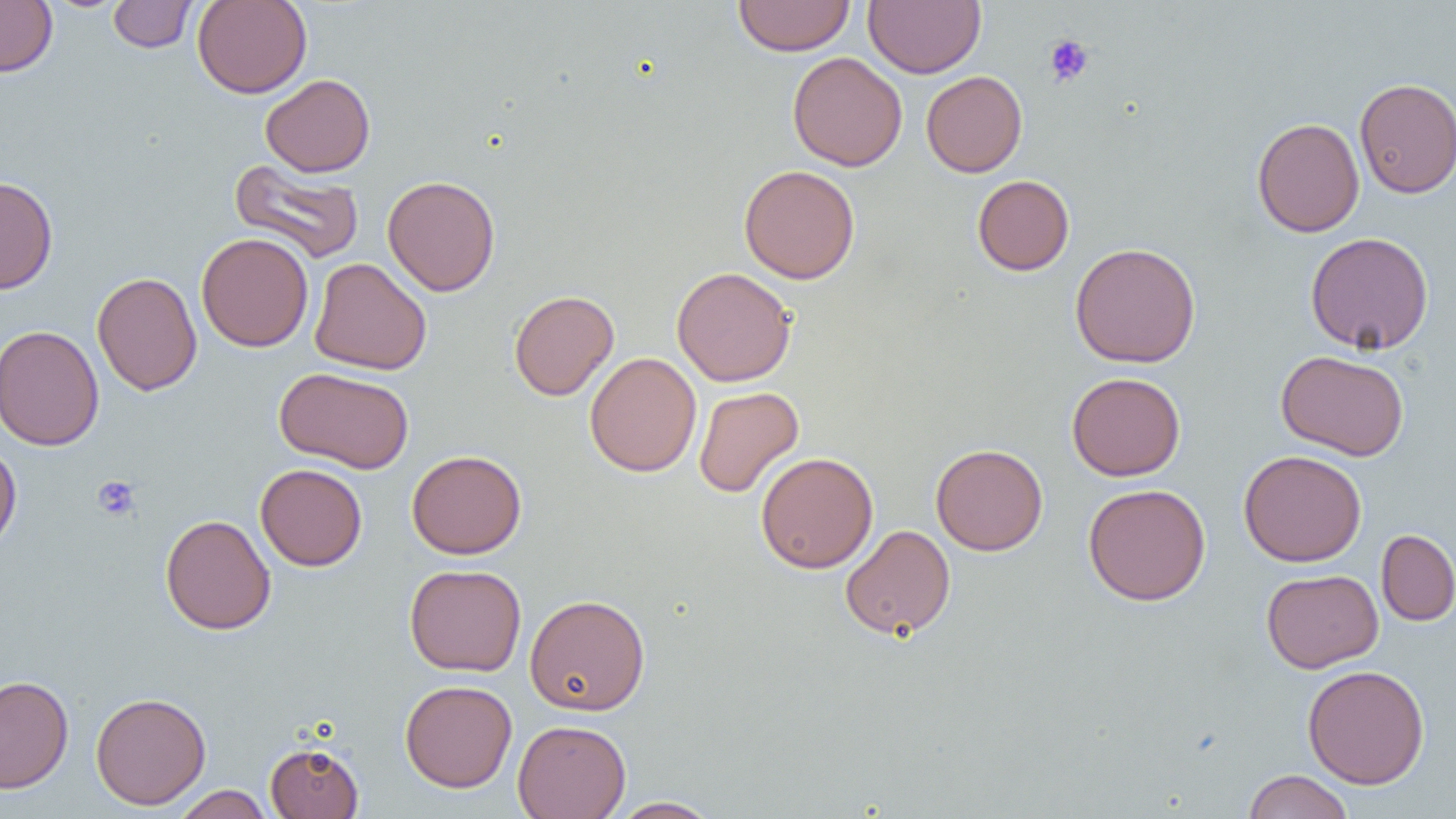 Approximate bounding boxes as (x1, y1, x2, y2) in pixels. Platelet locations: (1044, 34, 1093, 86), (92, 476, 141, 521). Uninfected red blood cell locations: (0, 0, 58, 77), (108, 0, 197, 53), (192, 0, 312, 98), (733, 0, 855, 56), (864, 0, 985, 78), (787, 52, 907, 171), (921, 71, 1028, 177), (261, 74, 375, 177), (1354, 78, 1456, 198), (1251, 117, 1365, 237), (229, 158, 365, 265), (739, 165, 860, 284), (383, 174, 500, 296), (972, 174, 1074, 275), (0, 176, 58, 295), (1304, 231, 1434, 355), (196, 233, 313, 352), (1070, 242, 1201, 367), (309, 257, 432, 376), (672, 267, 797, 387), (92, 271, 202, 396), (508, 290, 619, 401), (1, 324, 104, 451), (1277, 350, 1410, 461), (585, 352, 702, 477), (274, 366, 413, 474), (1067, 372, 1185, 481), (693, 386, 804, 498), (0, 443, 22, 555), (930, 443, 1048, 555), (1238, 449, 1367, 567), (406, 450, 527, 559), (755, 452, 878, 573), (255, 463, 367, 571), (1083, 483, 1211, 606), (160, 514, 276, 634), (840, 524, 956, 640), (1376, 529, 1456, 626), (404, 564, 527, 676), (1261, 568, 1383, 673), (524, 593, 651, 715), (1302, 664, 1430, 789), (0, 675, 74, 793), (400, 679, 517, 792), (90, 691, 211, 809), (513, 719, 631, 819), (265, 741, 364, 818), (1242, 769, 1354, 819), (172, 785, 273, 819), (608, 796, 721, 818). Slide-level diagnosis: negative for blood parasites. Thin blood film. Captured at 1000x magnification. One field of a larger specimen. Image is 1456×819 pixels. Light microscopy.